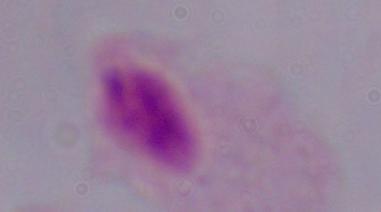

identification = trichomonad
modality = photomicrograph
magnification = 1000x